Outline platelets.
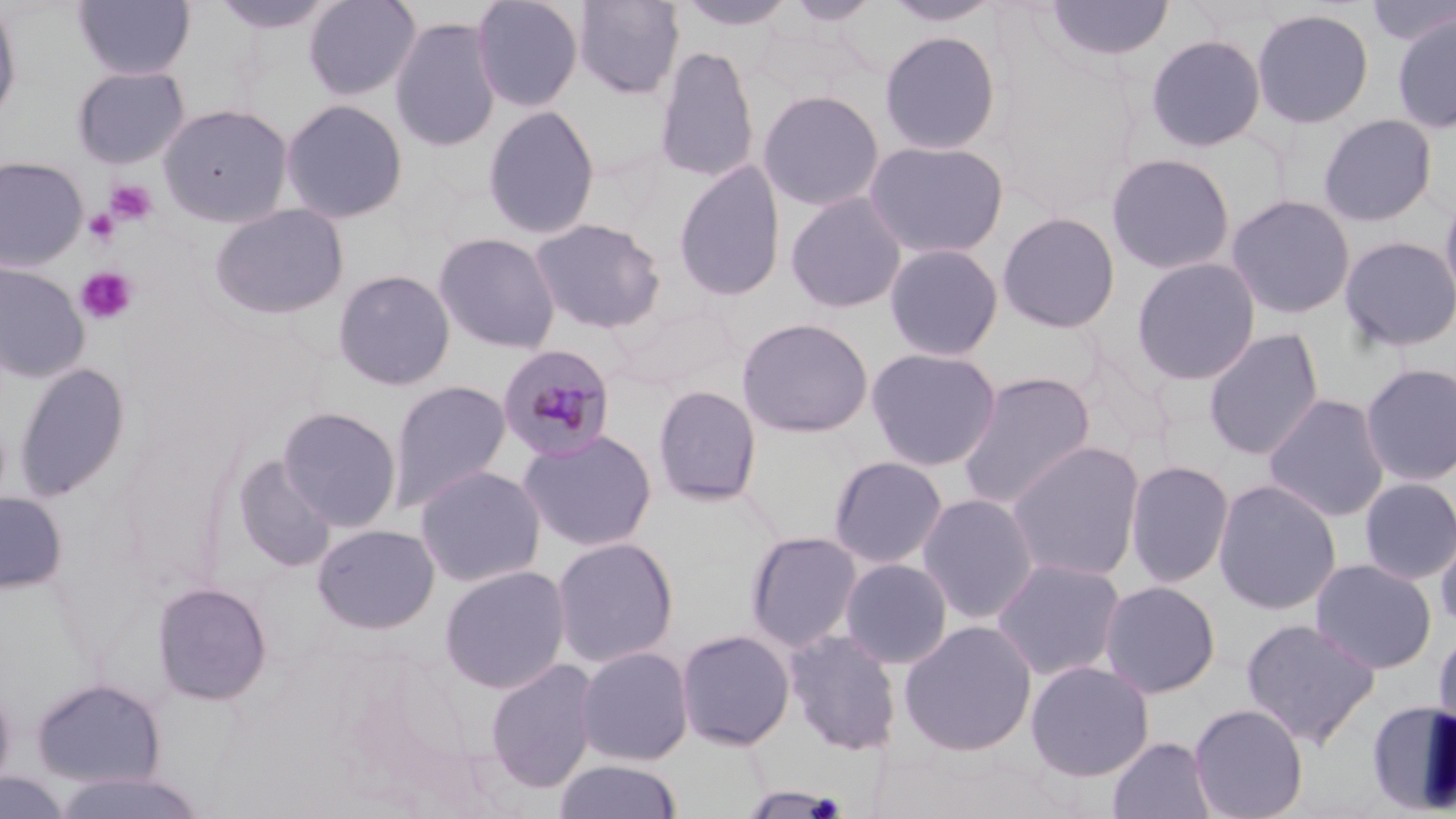
Approximate bounding boxes as named x1/y1/x2/y2 corners in pixels.
Platelets: (x1=105, y1=179, x2=159, y2=226), (x1=84, y1=209, x2=120, y2=246), (x1=75, y1=267, x2=138, y2=325).

Uninfected red blood cell locations: (x1=208, y1=0, x2=340, y2=35), (x1=302, y1=0, x2=421, y2=101), (x1=470, y1=0, x2=585, y2=112), (x1=572, y1=0, x2=685, y2=100), (x1=676, y1=0, x2=797, y2=32), (x1=782, y1=0, x2=883, y2=27), (x1=882, y1=0, x2=1003, y2=28), (x1=1043, y1=0, x2=1175, y2=63), (x1=0, y1=1, x2=23, y2=128), (x1=73, y1=1, x2=196, y2=81), (x1=1363, y1=1, x2=1456, y2=48), (x1=1251, y1=7, x2=1375, y2=129), (x1=1391, y1=11, x2=1456, y2=135), (x1=389, y1=16, x2=502, y2=152), (x1=879, y1=30, x2=1002, y2=155), (x1=1144, y1=33, x2=1267, y2=153), (x1=653, y1=45, x2=760, y2=184), (x1=71, y1=65, x2=191, y2=169), (x1=756, y1=89, x2=885, y2=211), (x1=279, y1=98, x2=409, y2=224), (x1=157, y1=102, x2=294, y2=226), (x1=482, y1=104, x2=601, y2=240), (x1=1318, y1=113, x2=1438, y2=227), (x1=863, y1=139, x2=1009, y2=260), (x1=1105, y1=152, x2=1237, y2=275), (x1=0, y1=156, x2=89, y2=271), (x1=673, y1=159, x2=787, y2=302), (x1=1439, y1=182, x2=1456, y2=315), (x1=785, y1=191, x2=907, y2=314), (x1=1224, y1=193, x2=1357, y2=320), (x1=208, y1=202, x2=349, y2=320), (x1=996, y1=211, x2=1122, y2=334), (x1=529, y1=218, x2=667, y2=334), (x1=433, y1=233, x2=561, y2=354), (x1=1339, y1=235, x2=1456, y2=353), (x1=884, y1=242, x2=1004, y2=362), (x1=1130, y1=256, x2=1262, y2=386), (x1=0, y1=262, x2=91, y2=383), (x1=332, y1=269, x2=456, y2=391), (x1=608, y1=299, x2=740, y2=393), (x1=736, y1=317, x2=874, y2=437), (x1=1203, y1=327, x2=1325, y2=461), (x1=865, y1=346, x2=1002, y2=471), (x1=13, y1=361, x2=132, y2=501), (x1=1359, y1=362, x2=1456, y2=488), (x1=957, y1=371, x2=1097, y2=511), (x1=388, y1=380, x2=511, y2=511), (x1=652, y1=384, x2=762, y2=506), (x1=1263, y1=393, x2=1391, y2=522), (x1=276, y1=406, x2=403, y2=532), (x1=517, y1=428, x2=658, y2=553), (x1=1005, y1=440, x2=1146, y2=582), (x1=231, y1=455, x2=337, y2=573), (x1=827, y1=455, x2=949, y2=570), (x1=1124, y1=459, x2=1235, y2=588), (x1=413, y1=464, x2=547, y2=588), (x1=1358, y1=476, x2=1456, y2=585), (x1=1212, y1=478, x2=1343, y2=615), (x1=0, y1=491, x2=68, y2=594), (x1=916, y1=493, x2=1040, y2=624), (x1=1434, y1=516, x2=1456, y2=635), (x1=312, y1=523, x2=440, y2=634), (x1=744, y1=530, x2=864, y2=653), (x1=551, y1=536, x2=679, y2=668), (x1=990, y1=557, x2=1127, y2=682), (x1=839, y1=558, x2=953, y2=669), (x1=1310, y1=558, x2=1438, y2=674), (x1=438, y1=564, x2=572, y2=694), (x1=1099, y1=580, x2=1222, y2=698), (x1=151, y1=581, x2=273, y2=706), (x1=1241, y1=618, x2=1381, y2=747), (x1=897, y1=620, x2=1038, y2=756), (x1=1432, y1=627, x2=1456, y2=742), (x1=675, y1=628, x2=795, y2=750), (x1=783, y1=629, x2=902, y2=756), (x1=575, y1=645, x2=694, y2=765), (x1=484, y1=658, x2=599, y2=794), (x1=1024, y1=660, x2=1155, y2=781), (x1=0, y1=674, x2=17, y2=795), (x1=30, y1=677, x2=166, y2=789), (x1=1365, y1=699, x2=1456, y2=815), (x1=1189, y1=702, x2=1309, y2=819), (x1=1107, y1=736, x2=1217, y2=819), (x1=554, y1=758, x2=684, y2=819), (x1=45, y1=769, x2=211, y2=819), (x1=0, y1=772, x2=74, y2=818), (x1=737, y1=786, x2=851, y2=818). Plasmodium malariae-infected red blood cell locations: (x1=497, y1=344, x2=617, y2=463). Slide-level diagnosis: Plasmodium malariae. Optical microscopy. Single field of view. Thin blood smear. 1000x magnification. May-Grünwald-Giemsa stain. Image is 1456×819 pixels.